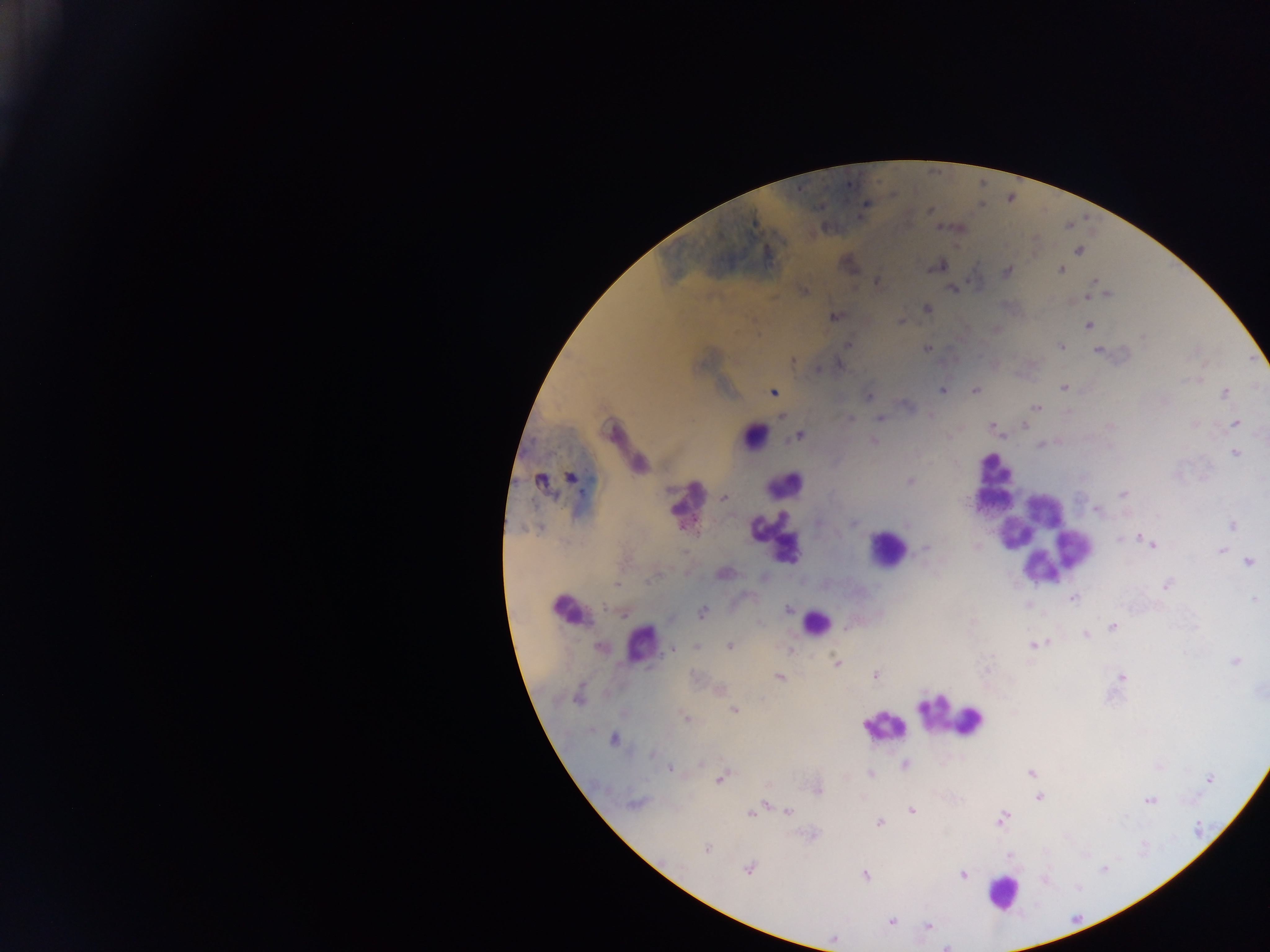

{
  "plasmodium_parasite_locations": "approximate centers as x y in pixels: 865 205; 930 211; 861 217; 940 227; 1078 251; 938 265; 1060 269; 1007 270; 876 283; 1093 283; 952 288; 804 291; 1105 295; 926 308; 834 316; 901 321; 1088 325; 995 329; 847 344; 1060 346; 927 348; 1099 350; 792 360; 994 363; 839 364; 819 369; 1200 378; 1064 388; 941 390; 974 391; 1225 392; 772 393; 868 396; 1163 401; 1037 407; 931 416; 879 418; 850 419; 1234 423; 1195 424; 992 426; 1024 426; 799 435; 1002 436; 873 441; 1041 444; 1235 453; 640 463; 570 477; 540 480; 909 482; 1123 494; 725 498; 907 522; 1233 525; 1138 536; 1146 539; 1154 544; 976 547; 925 548; 1220 549; 1248 561; 724 573; 1166 585; 1073 597; 1255 598; 788 609; 701 612; 1112 627; 847 629; 1085 633; 1049 641; 729 645; 1033 645; 600 646; 696 646; 671 647; 789 649; 1235 660; 836 663; 875 674; 779 677; 1121 677; 718 690; 579 696; 733 710; 685 717; 613 739; 653 754; 701 763; 905 764; 671 768; 1030 772; 870 773; 720 778; 1209 780; 816 788; 1039 796; 1149 800; 634 803; 766 803; 911 811; 788 812; 751 813; 1002 818; 878 822; 707 848; 748 868; 864 874; 962 874; 892 922; 927 925; 833 940",
  "preparation": "thick blood smear",
  "field_of_view": "single",
  "leukocyte_locations": "approximate centers as x y in pixels: 755 435; 993 481; 785 487; 686 503; 1008 512; 1041 537; 774 539; 887 550; 1043 564; 568 611; 815 623; 641 643; 953 717; 885 725; 1002 892",
  "country": "Ghana",
  "image_size": "1270×952 pixels",
  "capture": "mobile-phone photograph through a microscope"
}